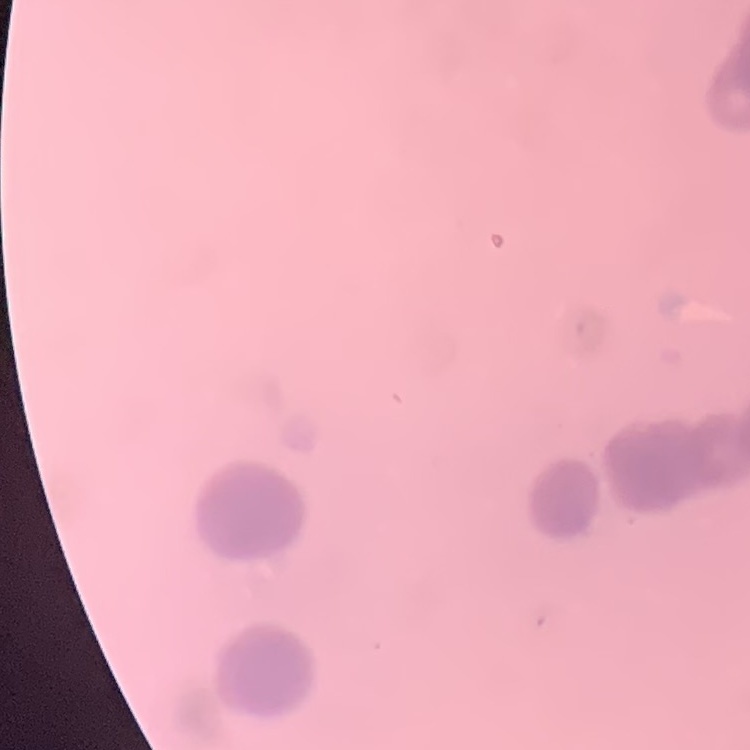

erythrocyte morphology = rouleaux formation
preparation = thin blood smear
stain = Field's or Giemsa
image type = square crop of a larger photomicrograph